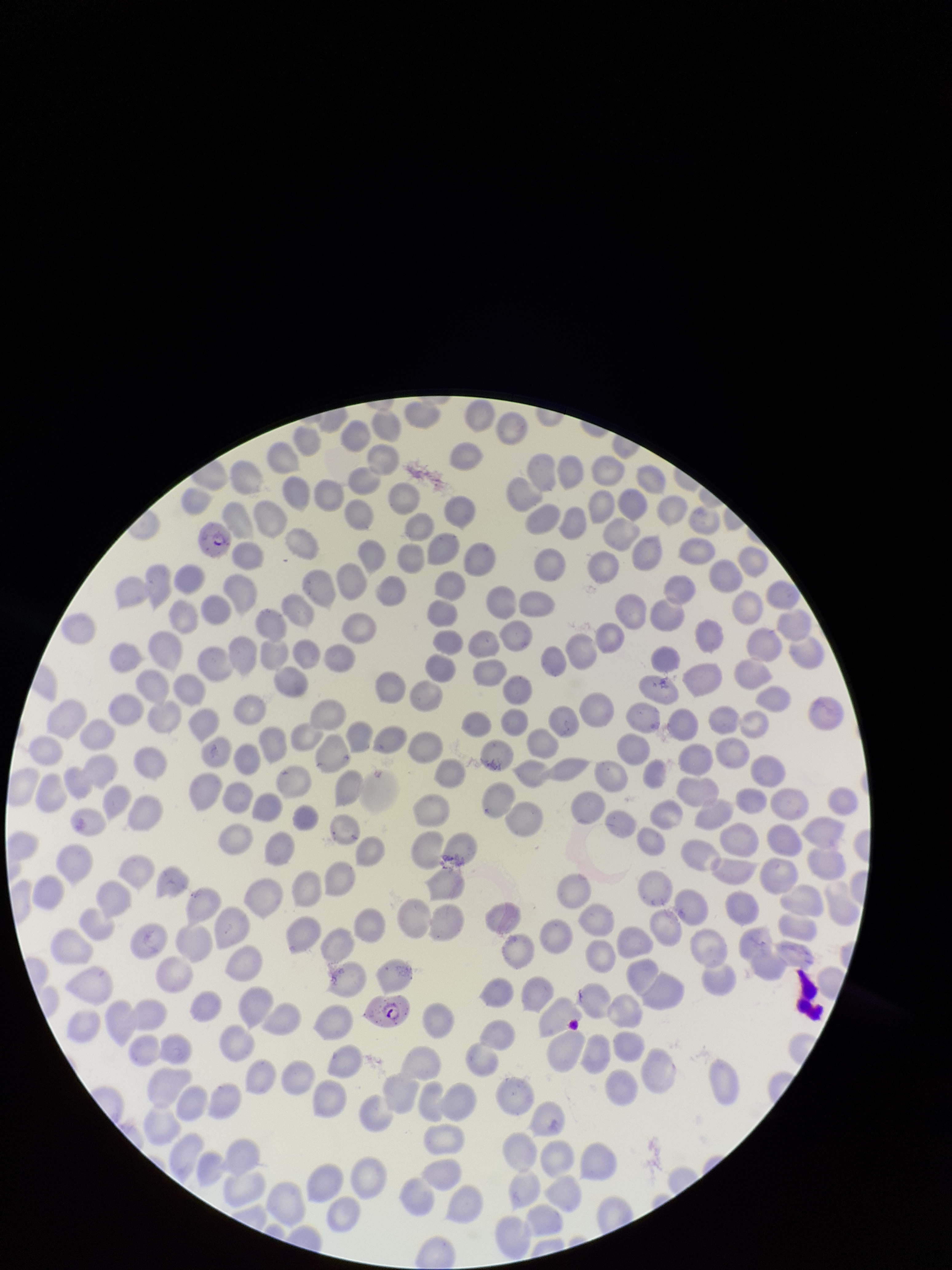

red blood cell count = 268
stain = Giemsa
species reported for this patient = Plasmodium falciparum
preparation = thin smear
parasitized red blood cell count = 2
image size = 952×1270 pixels
capture = smartphone photograph through the microscope eyepiece
parasitized red blood cells = identified
field of view = one from this slide
patient malaria status = infected